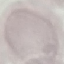
Summary:
  - Malaria status: uninfected
  - Capture: smartphone camera at the microscope eyepiece
  - Stain: Giemsa
  - Image type: cell patch, automatically extracted from a larger field of view and resized to 64 × 64 pixels
  - Preparation: thin smear